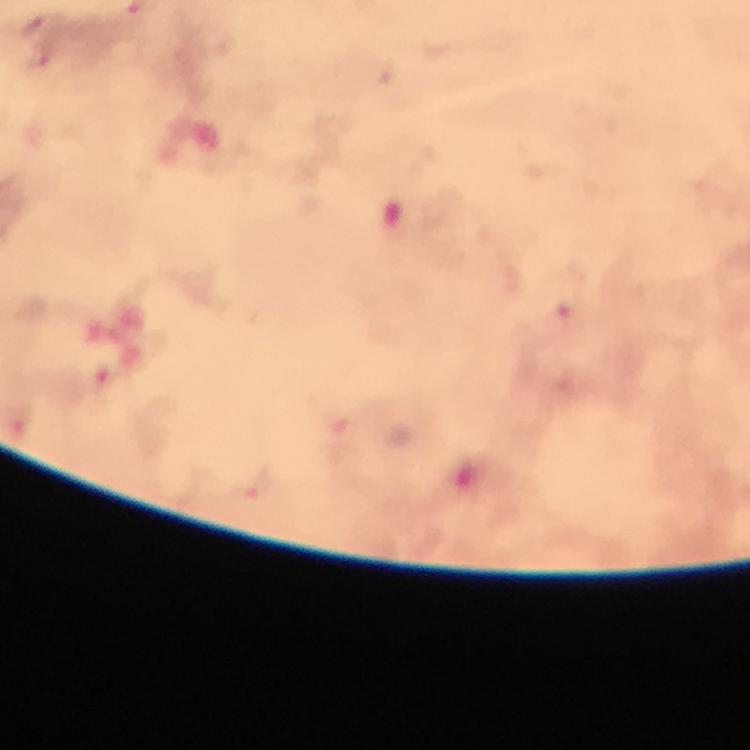

Approximate centers as {x, y} in pixels.
Summary:
  - Malaria parasite locations: {37, 24}, {40, 62}, {253, 488}
  - Image size: 750×750 pixels
  - Capture: smartphone camera through the microscope
  - Stain: Giemsa
  - Preparation: thick blood film
  - Cropped from: a single field of view
  - Context: from a diagnostic examination for malaria
  - Immersion oil: applied
  - Magnification: 100x